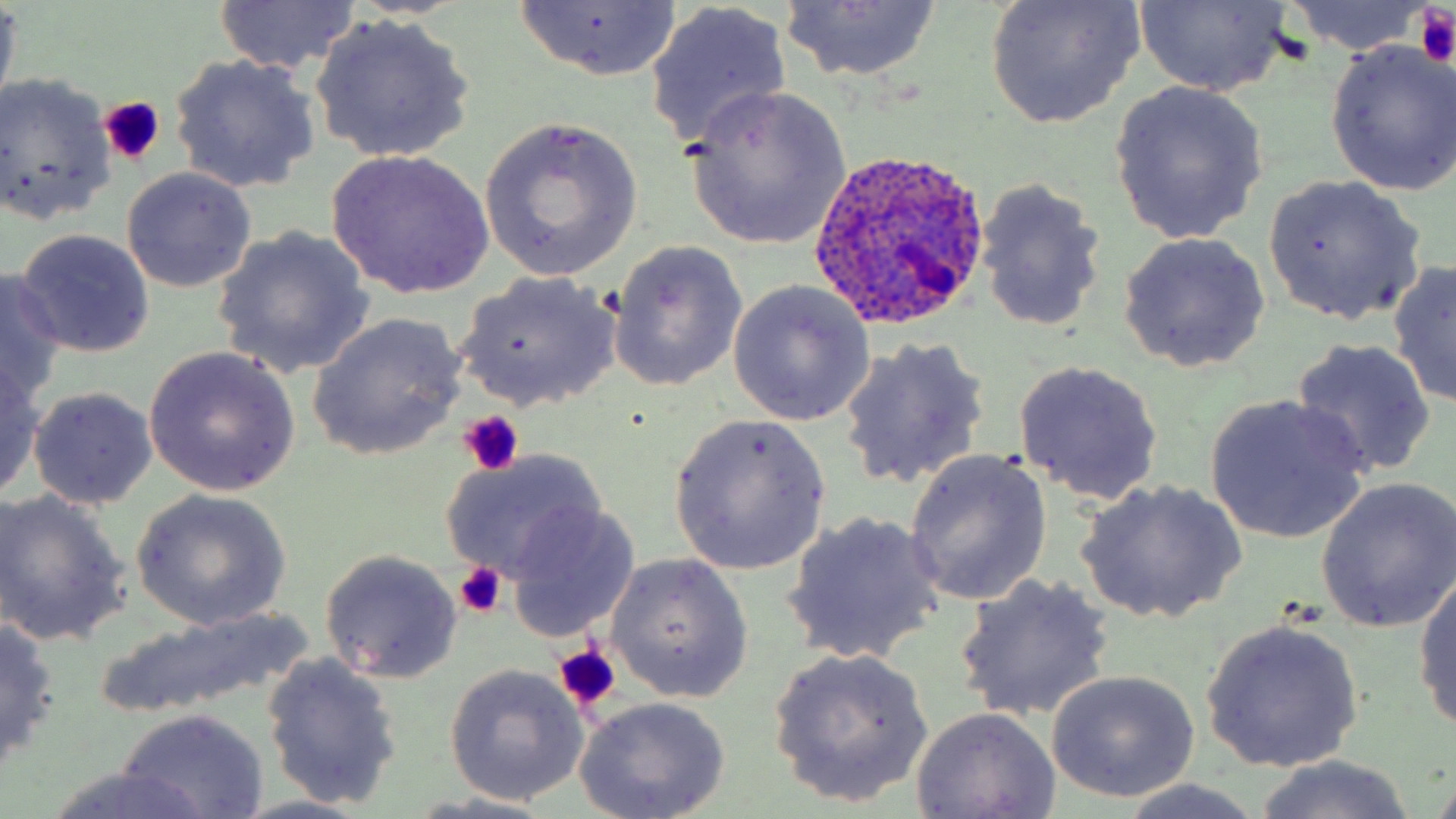
{
  "slide_level_diagnosis": "Plasmodium ovale",
  "preparation": "thin blood smear",
  "stain": "May-Grünwald-Giemsa",
  "image_size": "1456×819 pixels",
  "uninfected_red_blood_cell_locations": "approximate bounding boxes as (x1,y1)-(x2,y2) corner pairs in pixels: (211,0)-(360,77), (983,0)-(1145,126), (1133,0)-(1294,95), (1277,0)-(1439,56), (509,1)-(683,82), (778,1)-(943,82), (0,2)-(21,108), (646,5)-(794,150), (312,14)-(477,163), (1323,37)-(1456,197), (169,54)-(321,195), (0,73)-(116,226), (1109,80)-(1270,247), (684,86)-(852,249), (478,117)-(644,281), (327,149)-(494,298), (120,167)-(258,293), (1261,175)-(1426,327), (975,179)-(1107,334), (212,227)-(373,380), (15,229)-(155,359), (1117,231)-(1271,372), (608,241)-(747,391), (1388,260)-(1456,409), (0,270)-(67,407), (456,271)-(624,412), (728,281)-(878,427), (306,313)-(469,461), (837,337)-(991,493), (1290,339)-(1436,478), (144,346)-(301,497), (0,358)-(46,502), (1013,360)-(1164,507), (28,386)-(158,508), (1205,396)-(1369,544), (668,415)-(830,575), (904,447)-(1053,606), (440,451)-(606,584), (1314,477)-(1456,634), (1076,479)-(1245,625), (129,489)-(293,629), (0,491)-(132,647), (504,504)-(639,638), (781,510)-(947,666), (320,549)-(463,682), (607,554)-(753,703), (1413,566)-(1456,735), (952,575)-(1116,722), (90,611)-(315,720), (0,617)-(61,773), (1201,618)-(1364,773), (765,646)-(935,808), (260,652)-(402,810), (443,664)-(589,806), (1043,668)-(1201,805), (573,697)-(732,819), (910,706)-(1062,819), (116,709)-(269,818), (1251,756)-(1424,819), (43,769)-(216,819), (1108,779)-(1276,818), (404,793)-(572,818), (227,795)-(382,818)",
  "plasmodium_ovale_infected_red_blood_cell_locations": "approximate bounding boxes as (x1,y1)-(x2,y2) corner pairs in pixels: (810,145)-(991,334)",
  "magnification": "1000x",
  "field_of_view": "one of a larger specimen",
  "modality": "optical microscopy",
  "platelet_locations": "approximate bounding boxes as (x1,y1)-(x2,y2) corner pairs in pixels: (1414,9)-(1454,65), (99,96)-(164,166), (459,409)-(525,477), (451,561)-(506,620), (552,643)-(622,714)"
}